Identify the parasite.
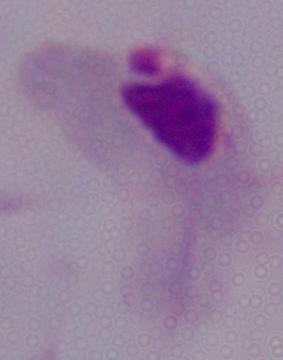
A trichomonad.

modality = micrograph
magnification = 1000x